Identify the blood parasite species.
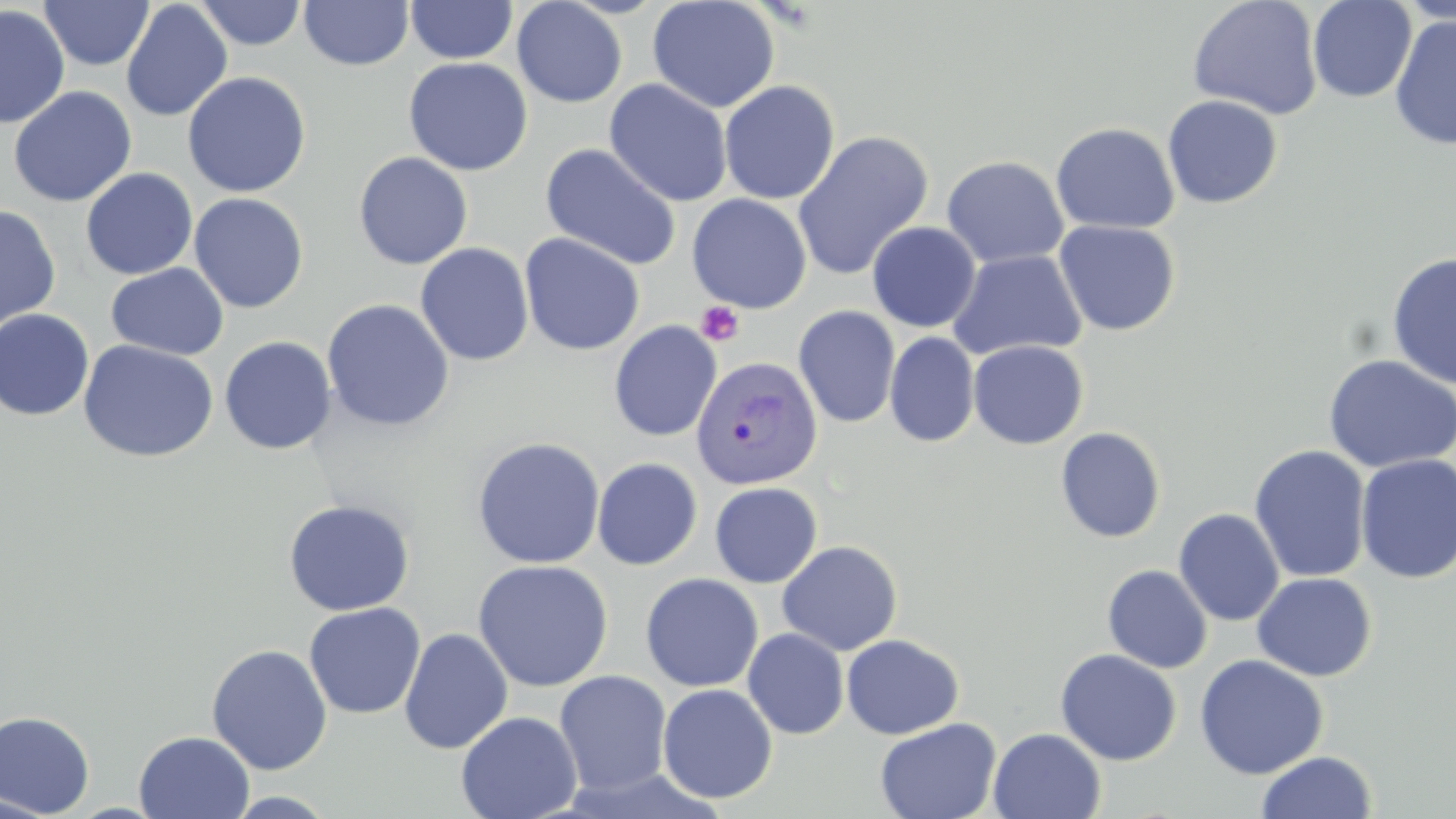
Plasmodium vivax.

Summary:
  - Coordinate format: approximate bounding boxes as named x1/y1/x2/y2 corners in pixels
  - Uninfected red blood cell locations: (x1=39, y1=0, x2=154, y2=71), (x1=71, y1=0, x2=195, y2=90), (x1=299, y1=0, x2=414, y2=71), (x1=647, y1=0, x2=780, y2=113), (x1=1187, y1=0, x2=1323, y2=120), (x1=1308, y1=0, x2=1417, y2=103), (x1=120, y1=1, x2=233, y2=122), (x1=194, y1=1, x2=309, y2=50), (x1=405, y1=1, x2=518, y2=64), (x1=511, y1=1, x2=627, y2=107), (x1=1397, y1=1, x2=1456, y2=28), (x1=0, y1=5, x2=70, y2=128), (x1=1389, y1=13, x2=1456, y2=151), (x1=402, y1=57, x2=534, y2=176), (x1=183, y1=71, x2=311, y2=198), (x1=604, y1=78, x2=733, y2=207), (x1=719, y1=80, x2=840, y2=204), (x1=8, y1=86, x2=137, y2=207), (x1=1162, y1=95, x2=1283, y2=209), (x1=1050, y1=122, x2=1180, y2=234), (x1=792, y1=130, x2=934, y2=281), (x1=541, y1=143, x2=682, y2=270), (x1=353, y1=151, x2=474, y2=270), (x1=941, y1=155, x2=1069, y2=268), (x1=80, y1=168, x2=198, y2=280), (x1=189, y1=192, x2=310, y2=314), (x1=686, y1=194, x2=811, y2=314), (x1=0, y1=204, x2=61, y2=333), (x1=1053, y1=220, x2=1181, y2=336), (x1=867, y1=222, x2=981, y2=332), (x1=519, y1=232, x2=645, y2=356), (x1=415, y1=242, x2=534, y2=366), (x1=948, y1=249, x2=1087, y2=361), (x1=1386, y1=251, x2=1456, y2=390), (x1=106, y1=263, x2=228, y2=361), (x1=321, y1=299, x2=455, y2=432), (x1=793, y1=305, x2=901, y2=428), (x1=0, y1=308, x2=95, y2=422), (x1=609, y1=320, x2=722, y2=442), (x1=885, y1=331, x2=980, y2=447), (x1=219, y1=336, x2=337, y2=455), (x1=77, y1=340, x2=219, y2=463), (x1=968, y1=340, x2=1089, y2=450), (x1=1322, y1=355, x2=1456, y2=473), (x1=1055, y1=426, x2=1166, y2=543), (x1=471, y1=436, x2=606, y2=569), (x1=1249, y1=445, x2=1371, y2=583), (x1=1354, y1=454, x2=1456, y2=584), (x1=592, y1=457, x2=703, y2=571), (x1=709, y1=481, x2=823, y2=588), (x1=283, y1=499, x2=414, y2=615), (x1=1173, y1=508, x2=1285, y2=626), (x1=776, y1=540, x2=903, y2=656), (x1=473, y1=559, x2=613, y2=691), (x1=1102, y1=565, x2=1213, y2=673), (x1=1252, y1=572, x2=1377, y2=681), (x1=640, y1=573, x2=764, y2=692), (x1=304, y1=602, x2=426, y2=719), (x1=399, y1=627, x2=513, y2=754), (x1=743, y1=628, x2=850, y2=739), (x1=841, y1=634, x2=964, y2=739), (x1=206, y1=643, x2=333, y2=775), (x1=1055, y1=648, x2=1182, y2=766), (x1=1194, y1=654, x2=1329, y2=779), (x1=554, y1=670, x2=672, y2=796), (x1=657, y1=683, x2=778, y2=804), (x1=0, y1=710, x2=96, y2=818), (x1=455, y1=711, x2=582, y2=819), (x1=874, y1=716, x2=1002, y2=819), (x1=988, y1=728, x2=1107, y2=818), (x1=133, y1=731, x2=255, y2=818), (x1=1256, y1=750, x2=1376, y2=818), (x1=224, y1=791, x2=340, y2=818), (x1=0, y1=794, x2=60, y2=818)
  - Platelet locations: (x1=695, y1=301, x2=744, y2=346)
  - Plasmodium vivax-infected red blood cell locations: (x1=690, y1=354, x2=823, y2=490)
  - Image size: 1456×819 pixels
  - Modality: light microscopy
  - Preparation: thin blood smear
  - Field of view: single
  - Magnification: 1000x
  - Stain: May-Grünwald-Giemsa